Classify this cell by malaria status.
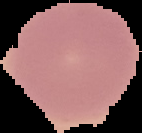
It is uninfected.

image type = segmented cell region on a black background
image size = 142×133 pixels
preparation = thin blood film